Classify this cell by malaria status.
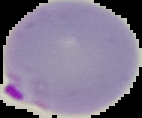
It is parasitized.

{
  "image_type": "segmented cell region with the area outside set to black",
  "preparation": "thin blood smear",
  "image_size": "142×118 pixels"
}